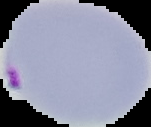

{
  "result": "malaria parasites detected",
  "image_type": "segmented cell region with the area outside set to black",
  "image_size": "151×127 pixels",
  "preparation": "thin blood film"
}